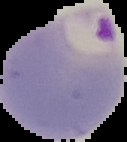
image size = 127×142 pixels
preparation = thin blood film
result = malaria parasites detected
image type = segmented cell region with the area outside set to black